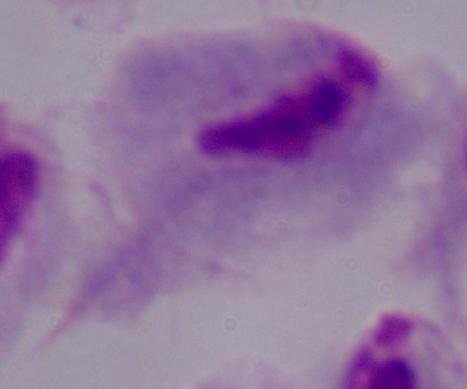

Summary:
  - Magnification: 1000x
  - Modality: photomicrograph
  - Identification: trichomonad